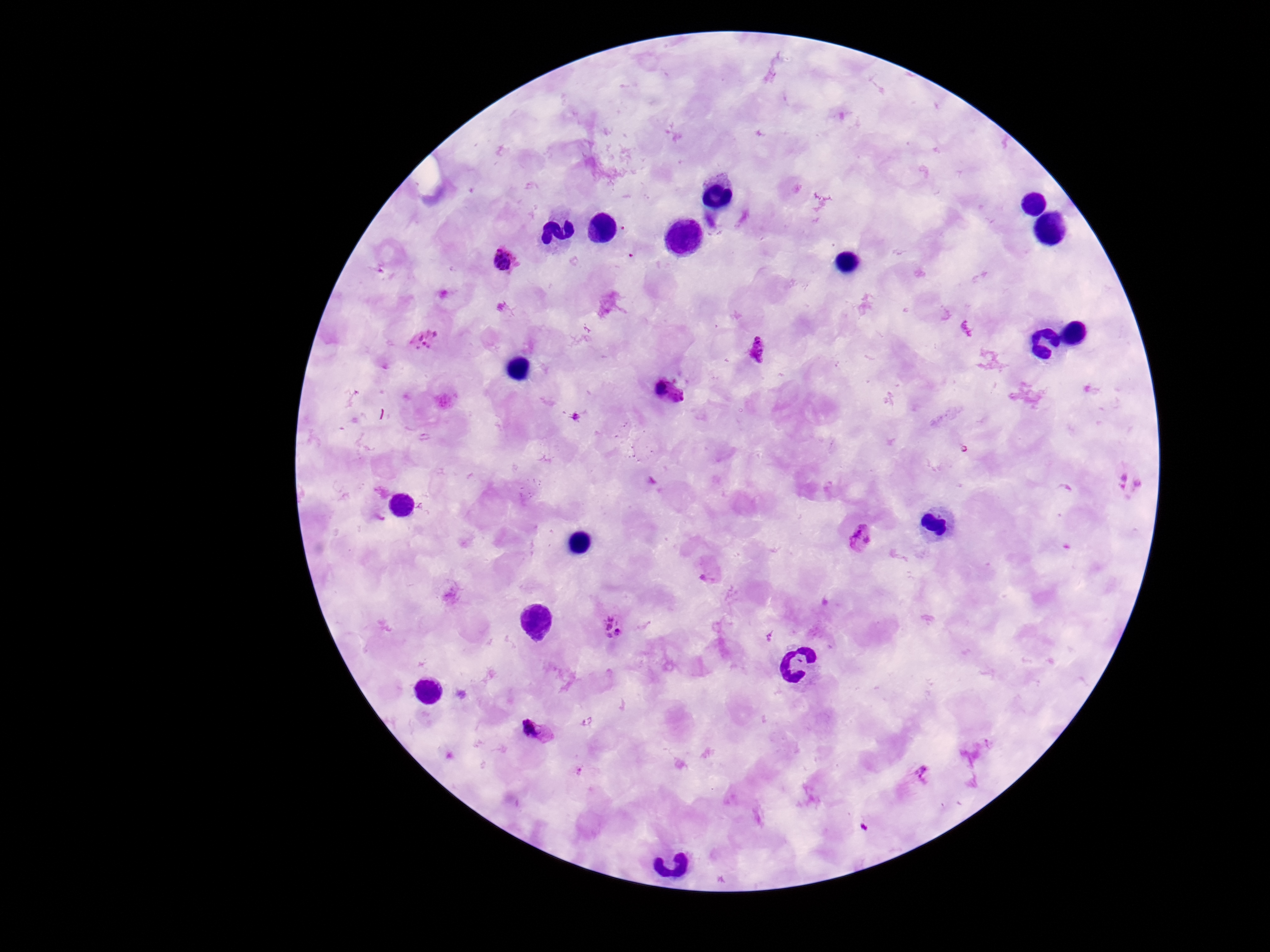

Approximate centers as (x, y) in pixels.
Summary:
  - Plasmodium parasite locations: (505, 263), (424, 341), (758, 349), (670, 392), (1128, 482), (863, 540), (709, 570), (612, 628), (536, 732), (923, 774)
  - Preparation: thick blood smear
  - Magnification: 100x
  - Field of view: single
  - Patient malaria status: positive
  - Stain: Giemsa
  - Capture: smartphone camera through the microscope eyepiece
  - Image size: 1270×952 pixels